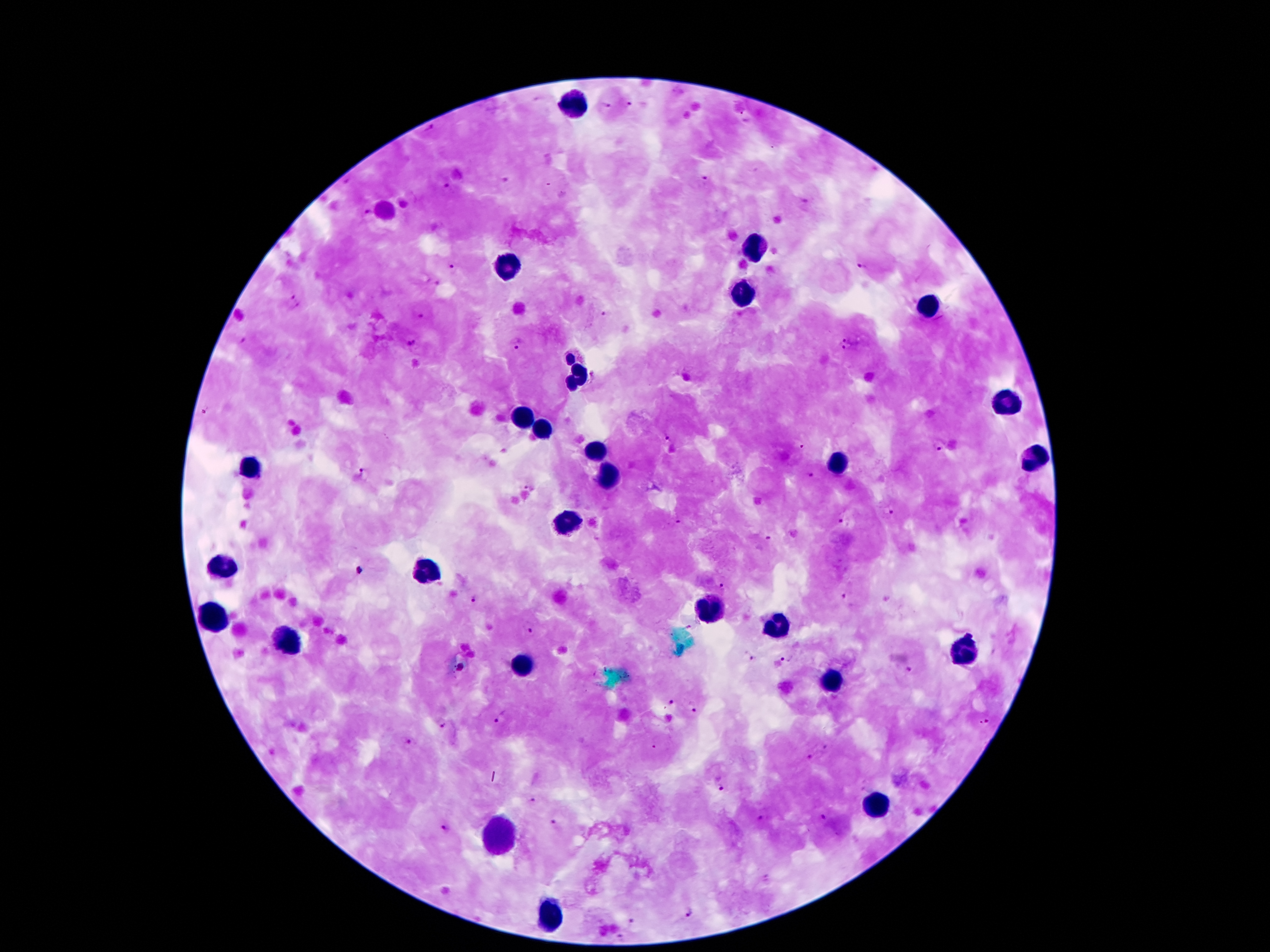

Approximate object centers, in pixels from the top-left corner. Plasmodium parasite locations: (x=537, y=100), (x=630, y=102), (x=605, y=105), (x=430, y=125), (x=705, y=177), (x=505, y=182), (x=444, y=187), (x=806, y=202), (x=365, y=213), (x=860, y=265), (x=453, y=269), (x=437, y=283), (x=289, y=296), (x=297, y=307), (x=607, y=316), (x=422, y=317), (x=846, y=340), (x=240, y=341), (x=410, y=342), (x=518, y=343), (x=845, y=350), (x=668, y=440), (x=939, y=445), (x=365, y=474), (x=809, y=476), (x=530, y=486), (x=889, y=513), (x=679, y=523), (x=844, y=523), (x=769, y=538), (x=359, y=571), (x=721, y=584), (x=843, y=597), (x=474, y=598), (x=690, y=627), (x=527, y=628), (x=748, y=656), (x=785, y=657), (x=911, y=669), (x=669, y=703), (x=692, y=707), (x=501, y=718), (x=985, y=723), (x=442, y=726), (x=410, y=743), (x=826, y=747), (x=811, y=756), (x=722, y=789), (x=532, y=799), (x=824, y=815), (x=761, y=819), (x=556, y=824), (x=445, y=829), (x=767, y=877), (x=689, y=911), (x=632, y=920), (x=618, y=937). Leukocyte locations: (x=570, y=106), (x=761, y=247), (x=507, y=264), (x=742, y=292), (x=931, y=304), (x=578, y=372), (x=1004, y=402), (x=524, y=420), (x=542, y=431), (x=597, y=453), (x=1034, y=460), (x=836, y=462), (x=248, y=469), (x=605, y=477), (x=566, y=521), (x=223, y=566), (x=425, y=572), (x=706, y=609), (x=213, y=617), (x=776, y=630), (x=286, y=638), (x=965, y=651), (x=524, y=664), (x=828, y=676), (x=872, y=804), (x=498, y=836), (x=547, y=911). Single field of view. Image is 1270×952 pixels. Giemsa stain. Patient malaria status: infected with Plasmodium falciparum. 100x magnification. Smartphone photograph taken through the microscope eyepiece. Thick blood smear.